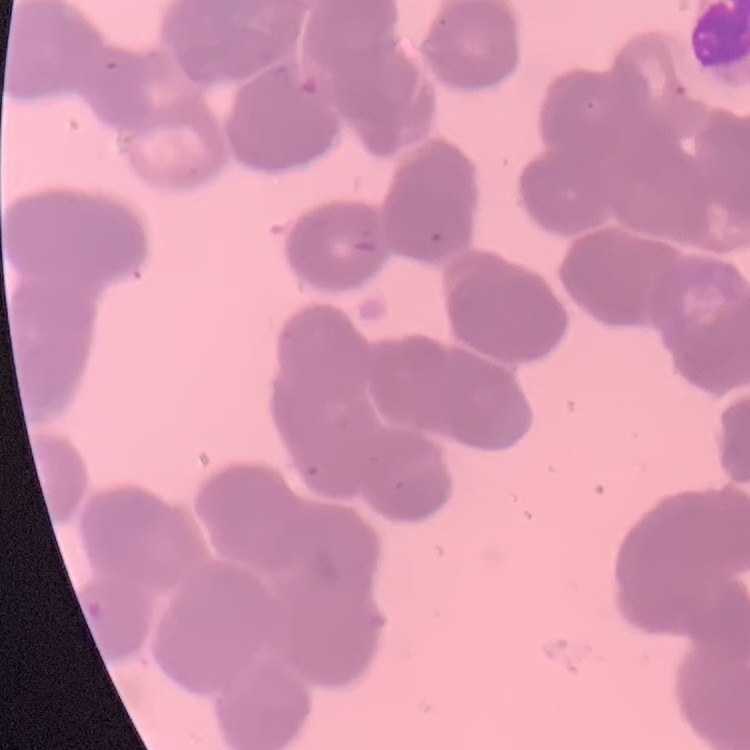
red_blood_cell_morphology: rouleaux formation
stain: Field's or Giemsa
preparation: thin blood smear
image_type: square crop of a larger photomicrograph